Locate every Plasmodium parasite and every leukocyte.
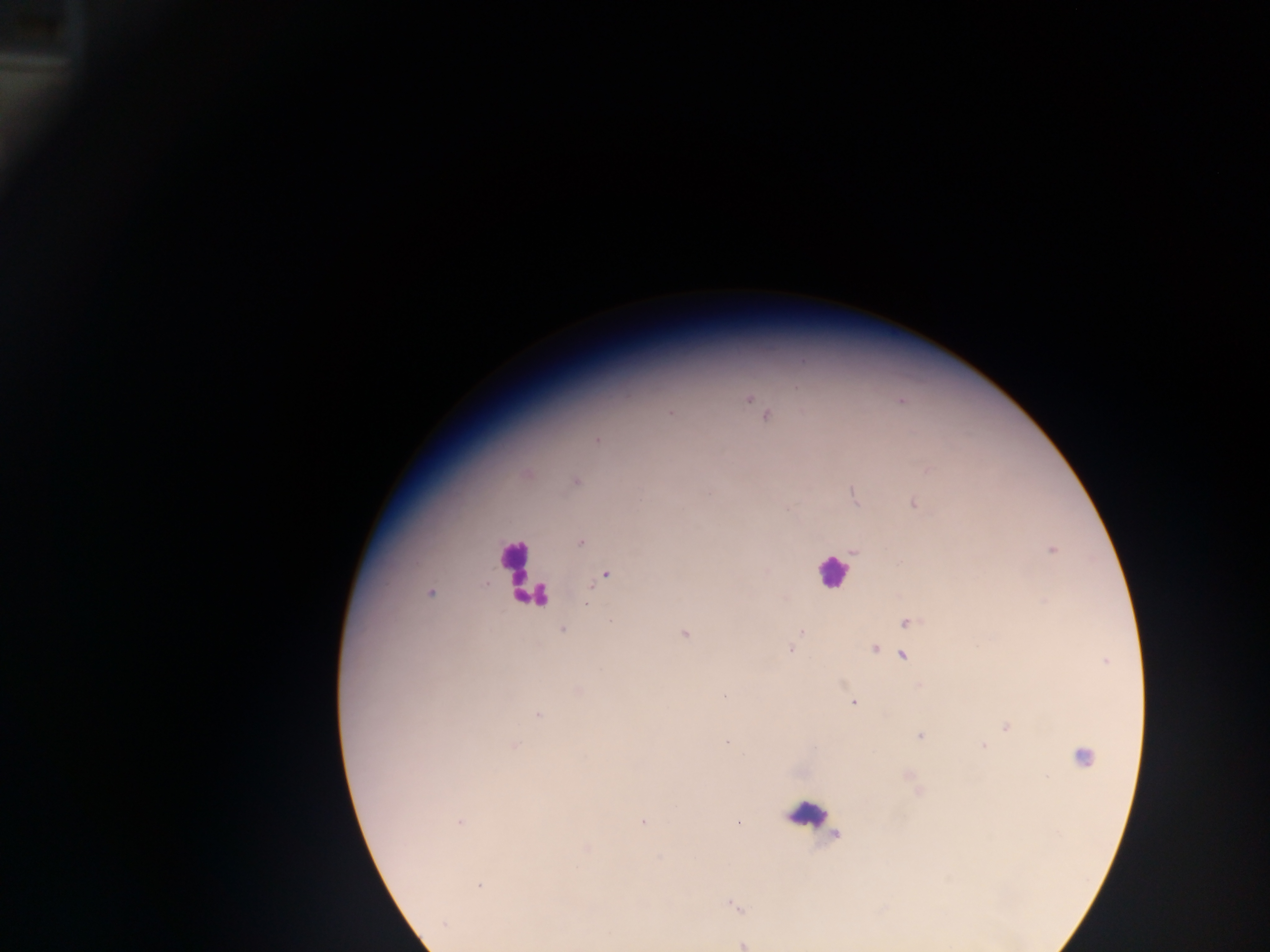
Approximate centers as {x, y} in pixels.
Plasmodium parasites: {750, 399}, {670, 413}, {765, 415}, {597, 440}, {928, 470}, {575, 481}, {853, 495}, {914, 504}, {580, 542}, {1052, 550}, {854, 551}, {606, 574}, {430, 593}, {587, 603}, {907, 622}, {563, 630}, {801, 632}, {685, 634}, {874, 648}, {791, 649}, {903, 656}, {578, 690}, {724, 696}, {854, 704}, {539, 715}, {1006, 726}, {919, 737}, {726, 743}, {515, 745}, {982, 745}, {642, 822}, {459, 823}, {738, 823}, {479, 887}, {735, 907}, {445, 924}, {743, 944}.
Leukocytes: {512, 563}, {831, 571}, {536, 595}, {1078, 757}, {812, 815}.

Summary:
  - Image size: 1270×952 pixels
  - Capture: mobile-phone photograph through a microscope
  - Preparation: thick blood smear
  - Country: Ghana
  - Field of view: single